Describe the morphology of the red blood cells.
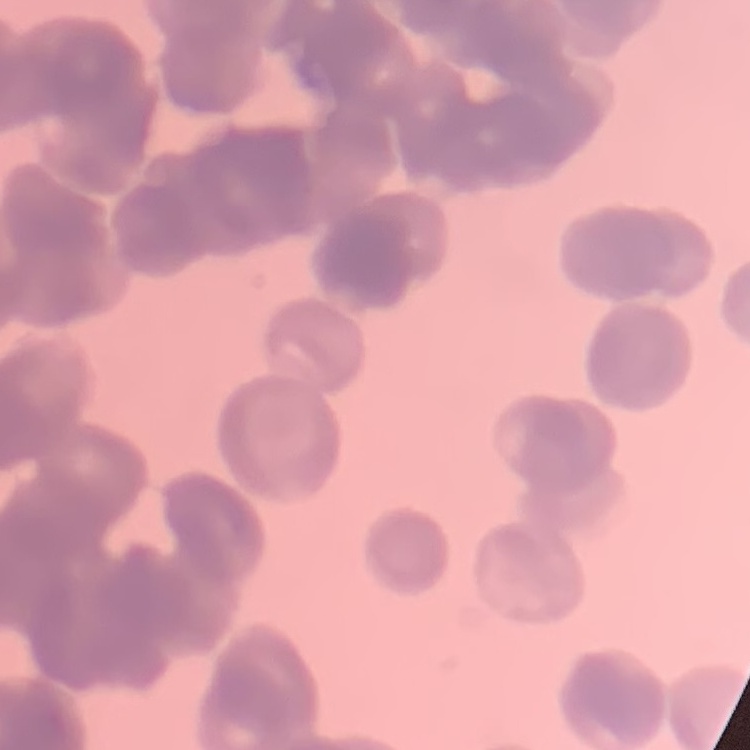
Rouleaux formation.

preparation = thin peripheral smear
image type = square crop of a larger photomicrograph
stain = Field's or Giemsa